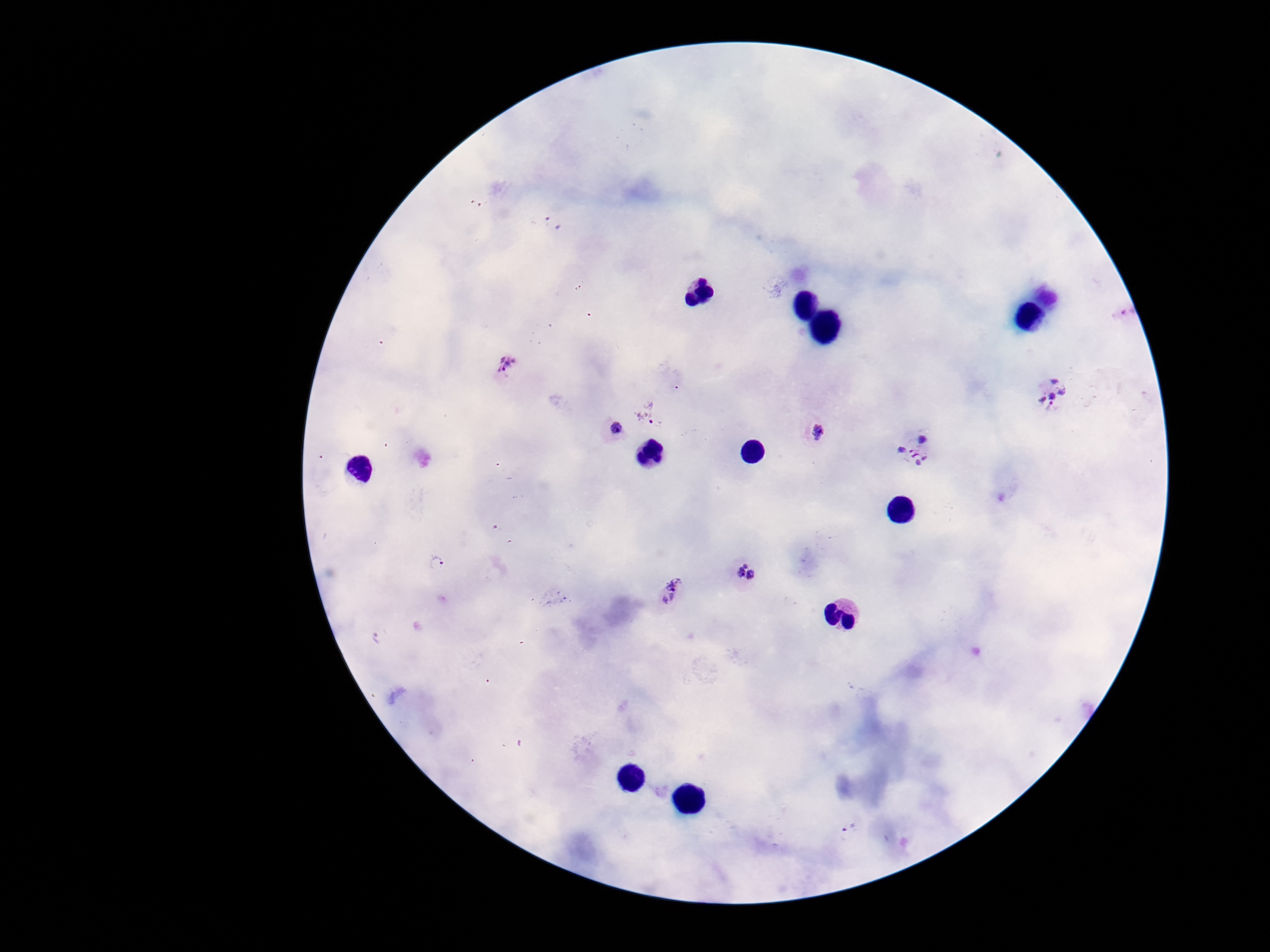

Approximate centers as [x, y] in pixels. Plasmodium parasite locations: [552, 223], [504, 368], [1050, 393], [647, 414], [610, 431], [813, 432], [917, 450], [438, 565], [748, 577], [668, 593], [376, 637], [849, 829]. One field from this slide. Patient malaria status: positive. Thick blood smear. Image is 1270×952 pixels. 100x magnification. Giemsa stain. Photographed through the microscope eyepiece with a smartphone camera.